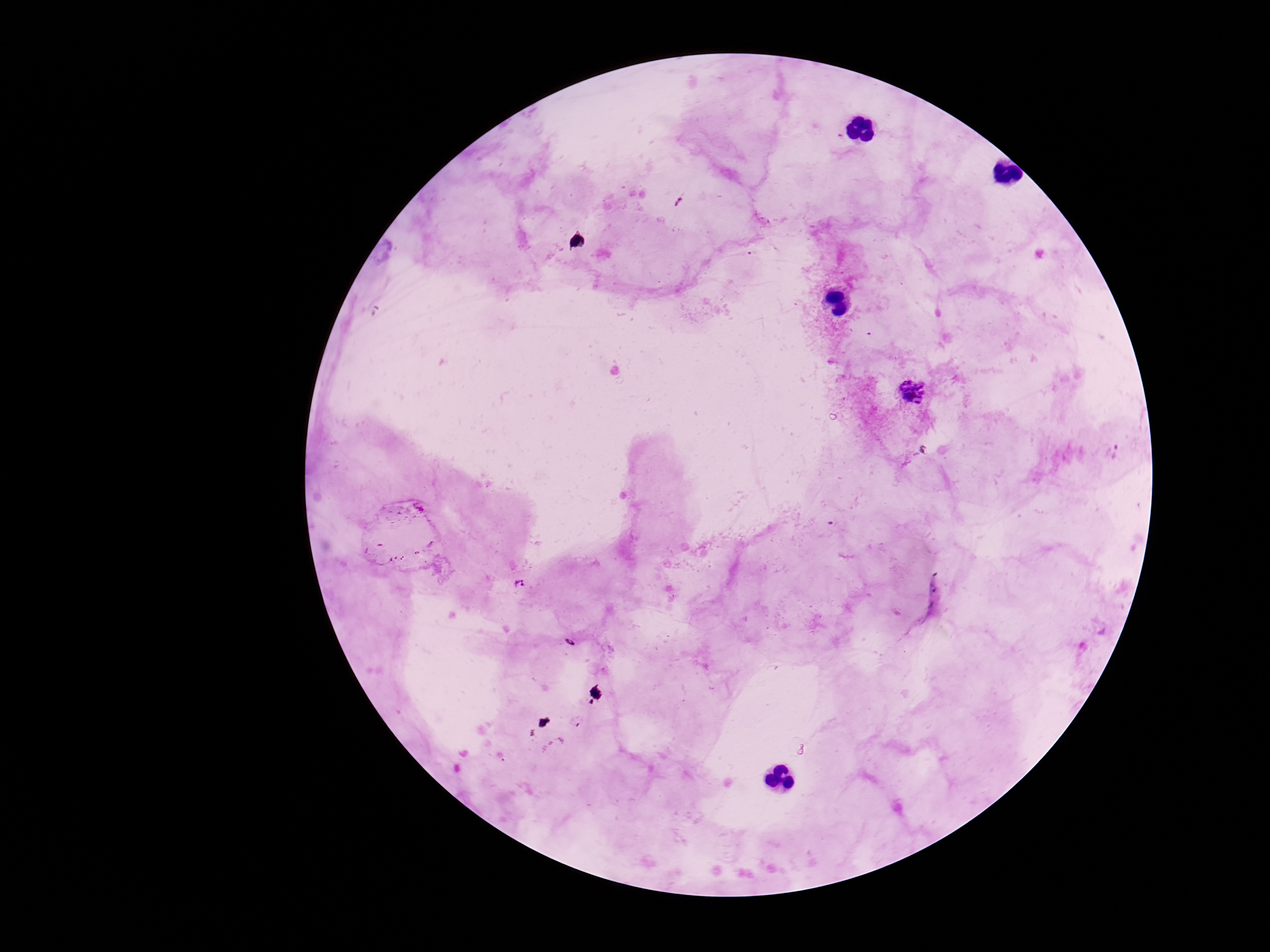

Approximate centers as [x, y] in pixels.
Summary:
  - Plasmodium parasite locations: [912, 391], [1113, 451], [520, 585], [570, 643]
  - Field of view: one from this slide
  - Patient malaria status: positive
  - Image size: 1270×952 pixels
  - Capture: smartphone camera through the microscope eyepiece
  - Stain: Giemsa
  - Magnification: 100x
  - Preparation: thick blood smear